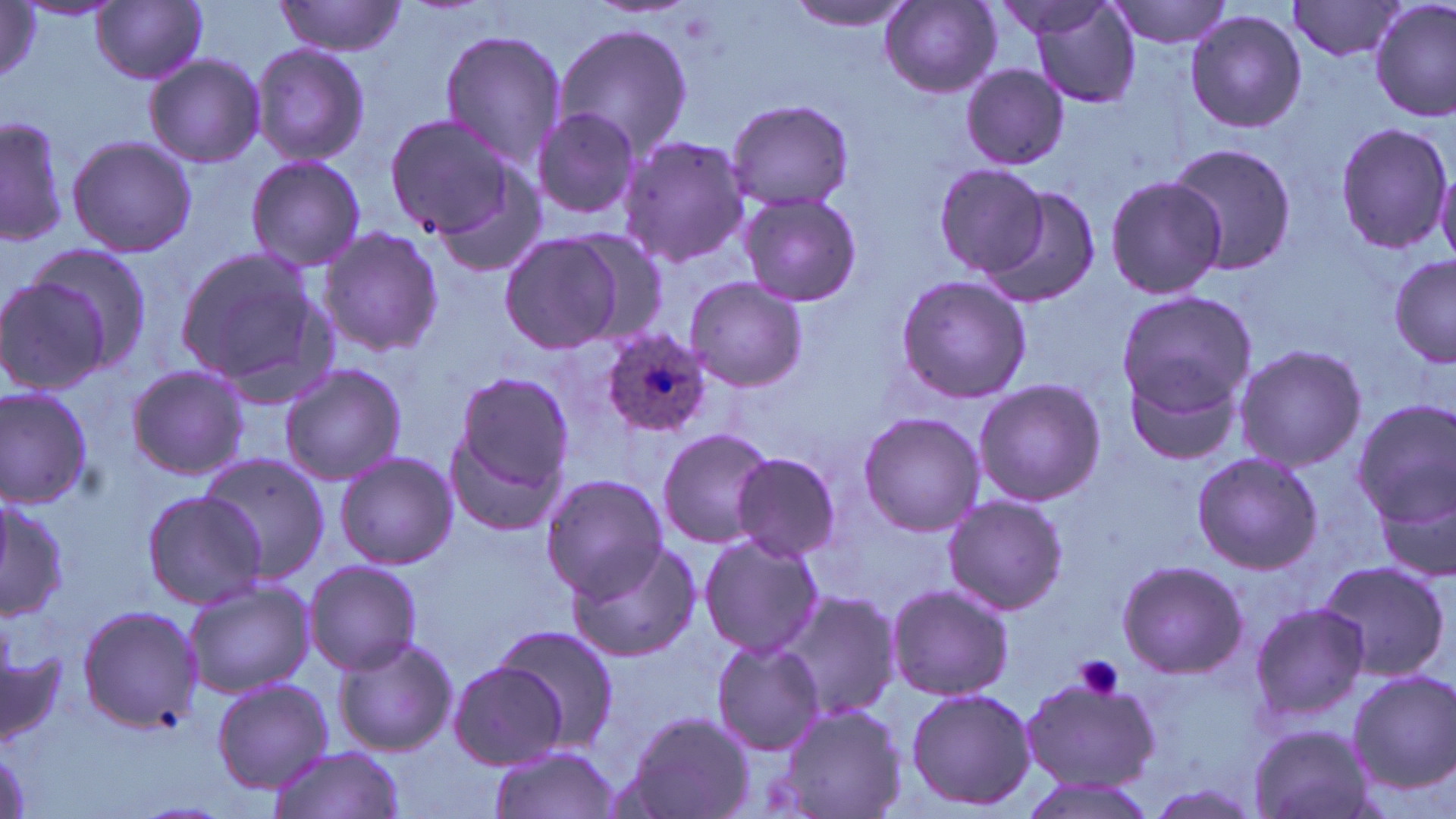
slide-level diagnosis = Plasmodium ovale
image size = 1456×819 pixels
preparation = thin blood smear
stain = May-Grünwald-Giemsa
modality = optical microscopy
field of view = one of a larger specimen
uninfected red blood cell locations = approximate bounding boxes as (x1,y1)-(x2,y2) corner pairs in pixels: (1014,0)-(1145,110), (1104,0)-(1237,50), (1371,0)-(1455,122), (92,1)-(208,83), (789,1)-(917,34), (1287,1)-(1409,62), (274,2)-(407,57), (880,2)-(1003,98), (2,3)-(42,85), (1183,8)-(1309,135), (552,22)-(695,159), (438,28)-(566,175), (250,42)-(371,166), (143,53)-(264,168), (959,63)-(1071,170), (724,99)-(856,210), (530,107)-(643,224), (387,113)-(526,246), (1,115)-(67,247), (1333,121)-(1455,253), (66,133)-(197,260), (619,133)-(750,268), (1163,141)-(1298,275), (245,154)-(366,272), (935,162)-(1050,275), (1103,174)-(1226,300), (974,181)-(1105,307), (738,190)-(863,309), (316,227)-(446,358), (558,228)-(671,349), (499,232)-(625,354), (23,243)-(152,369), (171,245)-(335,402), (1389,252)-(1455,370), (894,273)-(1031,405), (682,277)-(808,391), (0,278)-(112,395), (1114,289)-(1257,424), (1232,344)-(1365,472), (1121,361)-(1247,468), (124,362)-(253,481), (280,362)-(408,487), (450,369)-(575,499), (971,378)-(1105,507), (0,385)-(94,509), (1352,398)-(1456,529), (855,412)-(986,536), (446,424)-(565,538), (655,426)-(776,549), (332,451)-(459,570), (1190,451)-(1322,574), (728,452)-(843,558), (197,453)-(331,580), (540,473)-(668,599), (1376,479)-(1456,587), (140,489)-(266,606), (941,494)-(1066,614), (0,495)-(68,624), (698,533)-(825,659), (563,538)-(701,662), (1315,557)-(1451,682), (1115,558)-(1247,680), (301,560)-(425,676), (181,579)-(315,697), (884,582)-(1015,703), (781,590)-(901,720), (1246,602)-(1371,723), (75,604)-(203,731), (479,629)-(617,756), (329,633)-(456,757), (0,638)-(72,752), (710,640)-(825,756), (446,660)-(568,770), (1345,669)-(1455,790), (1019,678)-(1162,792), (212,679)-(333,791), (904,686)-(1036,813), (774,702)-(909,819), (623,712)-(754,819), (1245,724)-(1375,819), (488,744)-(623,819), (266,745)-(406,818), (1015,775)-(1159,819), (1142,781)-(1263,819)
platelet locations = approximate bounding boxes as (x1,y1)-(x2,y2) corner pairs in pixels: (1075,654)-(1126,700)
Plasmodium ovale-infected red blood cell locations = approximate bounding boxes as (x1,y1)-(x2,y2) corner pairs in pixels: (598,331)-(714,438)
magnification = 1000x